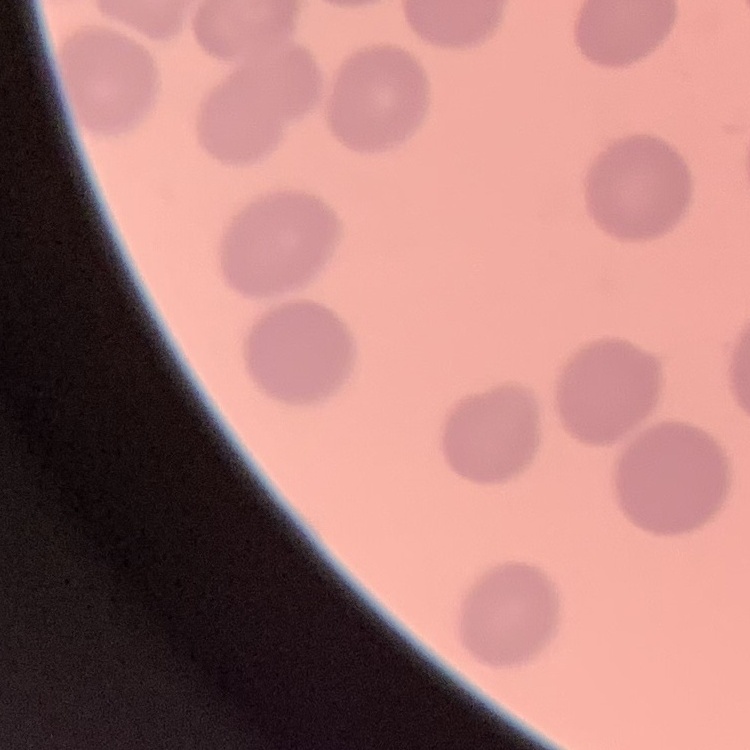

Summary:
  - Red blood cell morphology: no rouleaux formation
  - Stain: Field's or Giemsa
  - Image type: square crop of a larger photomicrograph
  - Preparation: thin blood film